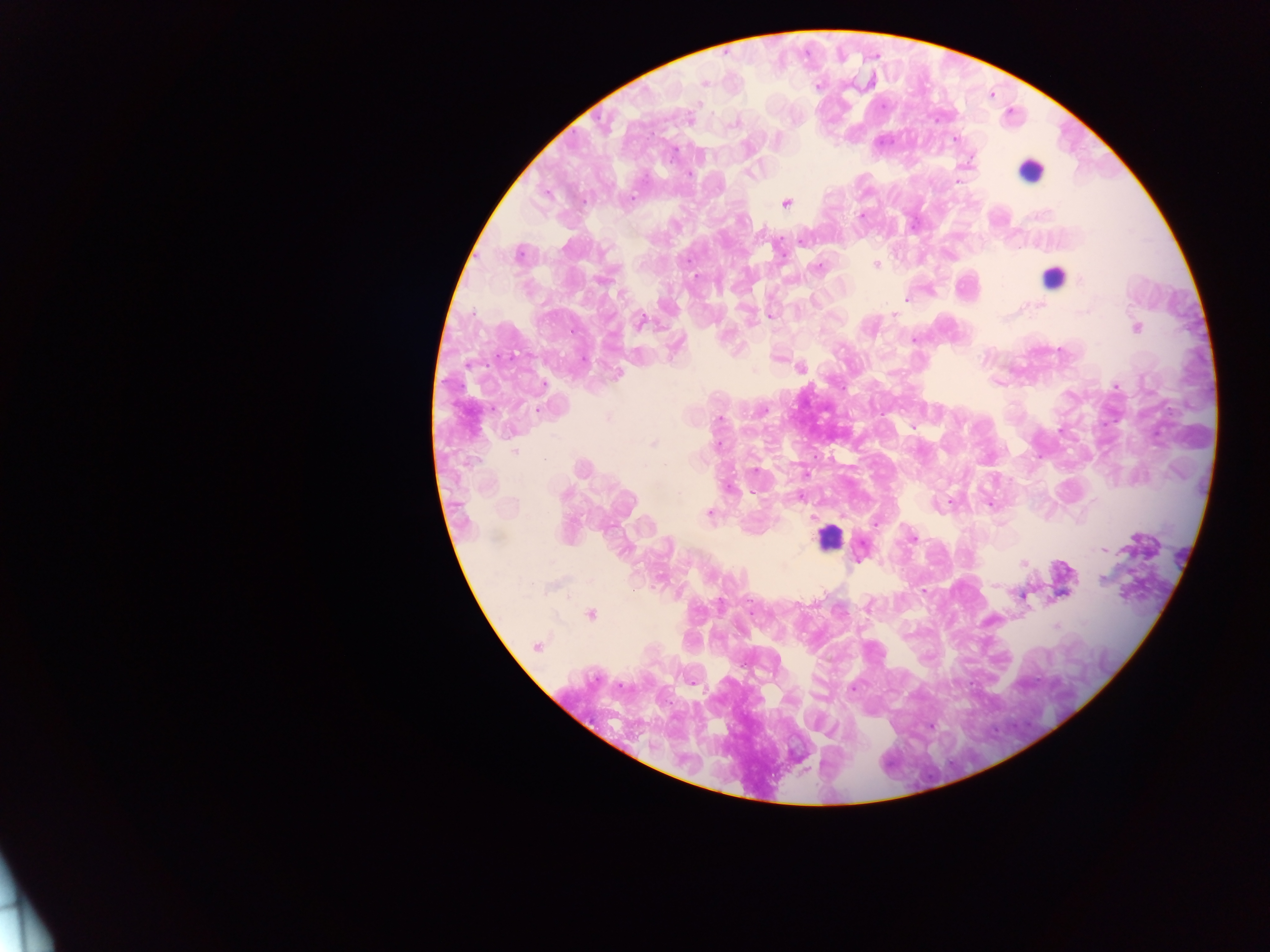

Approximate centers as {x, y} in pixels. Leukocyte locations: {1028, 172}, {1049, 278}, {829, 533}. Plasmodium parasite locations: {705, 83}, {872, 83}, {820, 88}, {699, 104}, {940, 117}, {735, 122}, {955, 136}, {778, 138}, {674, 147}, {699, 152}, {754, 171}, {690, 173}, {786, 202}, {861, 215}, {811, 265}, {877, 266}, {695, 275}, {1073, 277}, {617, 293}, {907, 296}, {1038, 304}, {1082, 312}, {769, 315}, {894, 316}, {1006, 318}, {649, 324}, {1136, 327}, {914, 339}, {734, 349}, {512, 352}, {471, 363}, {801, 369}, {617, 372}, {541, 389}, {535, 409}, {762, 410}, {719, 419}, {1059, 429}, {719, 441}, {652, 443}, {515, 452}, {664, 466}, {581, 469}, {755, 470}, {569, 492}, {756, 494}, {938, 501}, {944, 505}, {709, 512}, {913, 536}, {1103, 551}, {784, 564}, {1023, 564}, {1104, 578}, {994, 585}, {568, 594}, {590, 614}, {1056, 626}, {741, 633}, {536, 645}, {626, 685}, {855, 687}, {933, 725}. Sample from Ghana. Thick blood smear. Photographed through a microscope with a mobile-phone camera. One field of view. Image is 1270×952 pixels.